Report the malaria status of this cell.
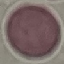

It is uninfected.

Thin blood film. Acquired by smartphone through the microscope eyepiece. Automatically extracted cell patch, resized to 64 × 64 pixels. Giemsa-stained preparation.